Identify the parasite.
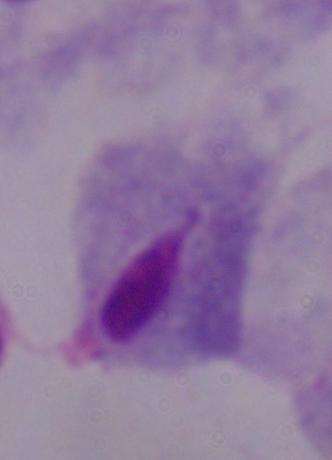

A trichomonad.

magnification = 1000x
modality = photomicrograph